Comment on the morphology of the erythrocytes.
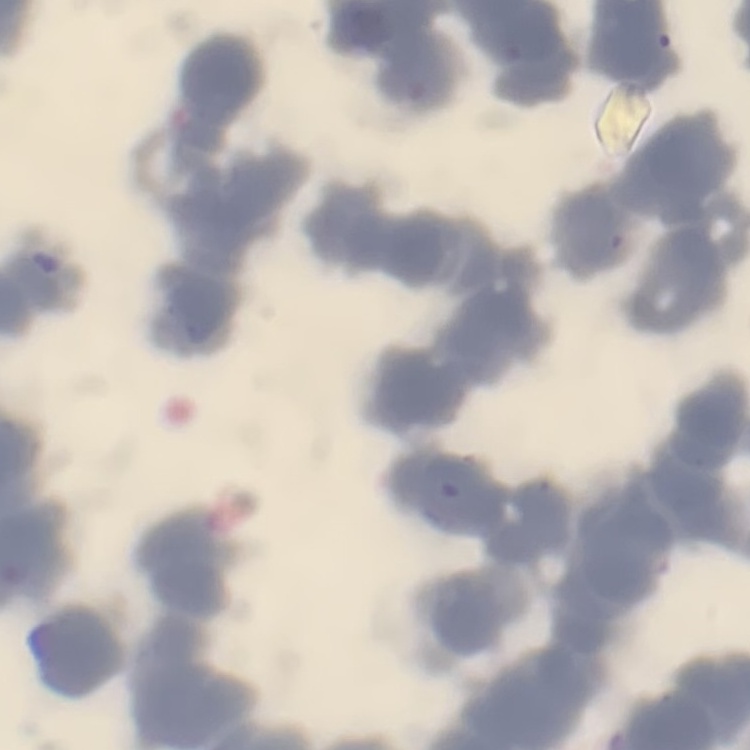

Rouleaux formation.

preparation = thin peripheral smear
stain = Field's or Giemsa
image type = one tile cut from a larger photomicrograph